Evaluate for parasitized red blood cells.
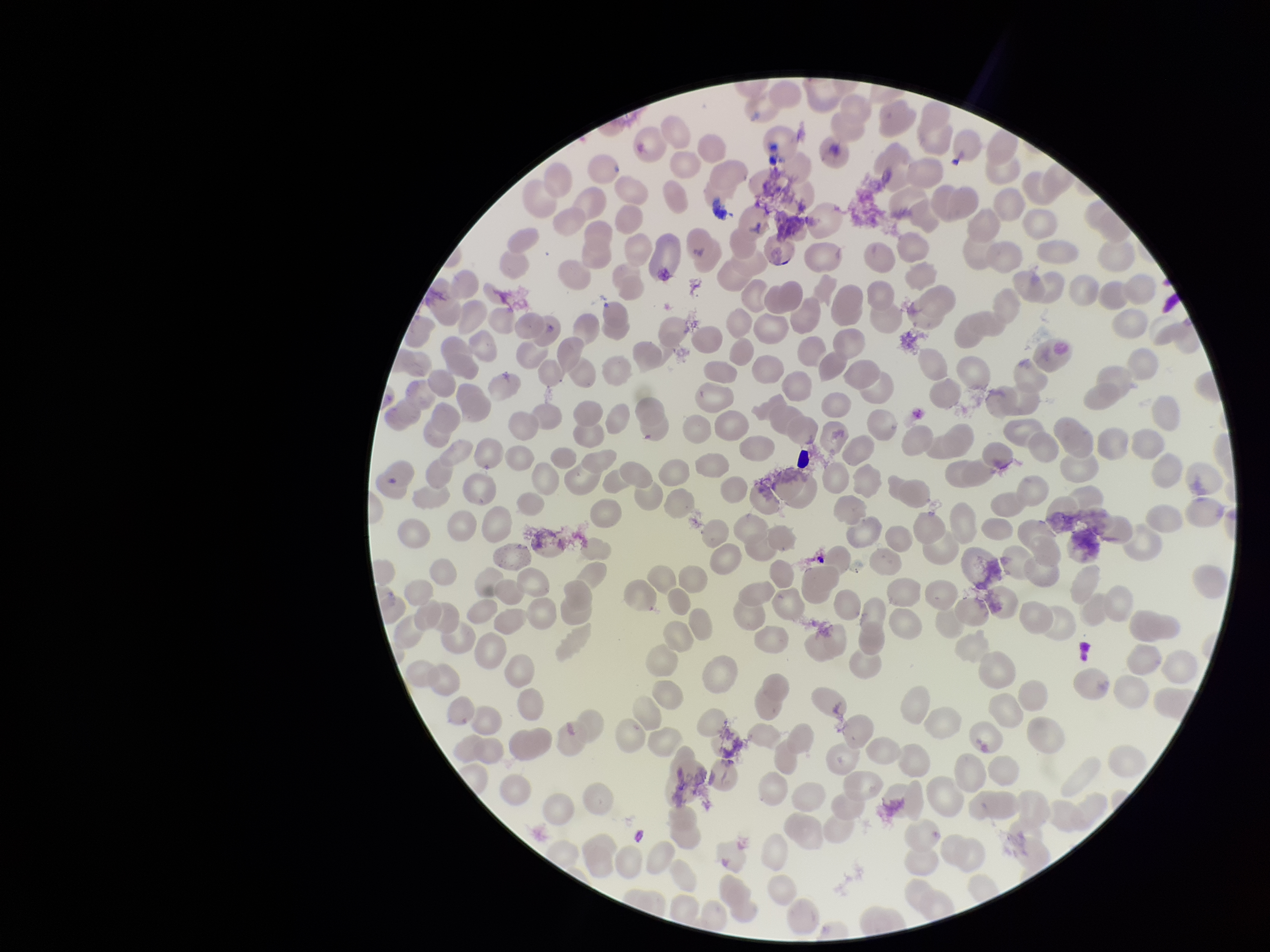

None seen.

Patient malaria status: positive. Image is 1270×952 pixels. Red blood cell count: 243. Species reported for this patient: Plasmodium falciparum. Preparation: thin smear. Parasitized red blood cell count: 0. Photographed through the microscope eyepiece with a smartphone camera. Stained with Giemsa. One field from this slide.